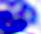
Summary:
  - Identification: leukocyte
  - Modality: micrograph
  - Magnification: 400x